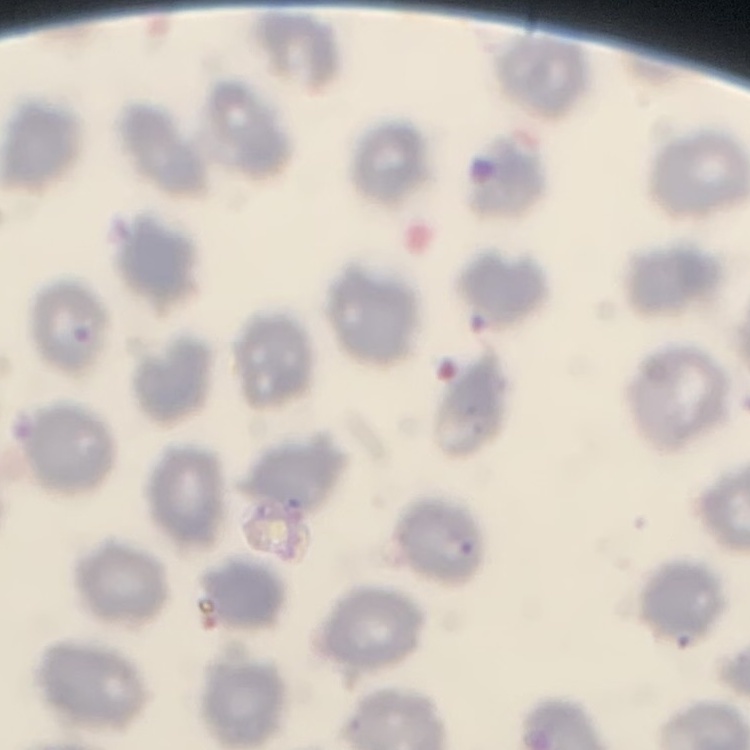
The red blood cells show no rouleaux formation. Thin peripheral smear. Stained with either Field's or Giemsa. One tile cut from a larger photomicrograph.